Locate every blood parasite and identify its species.
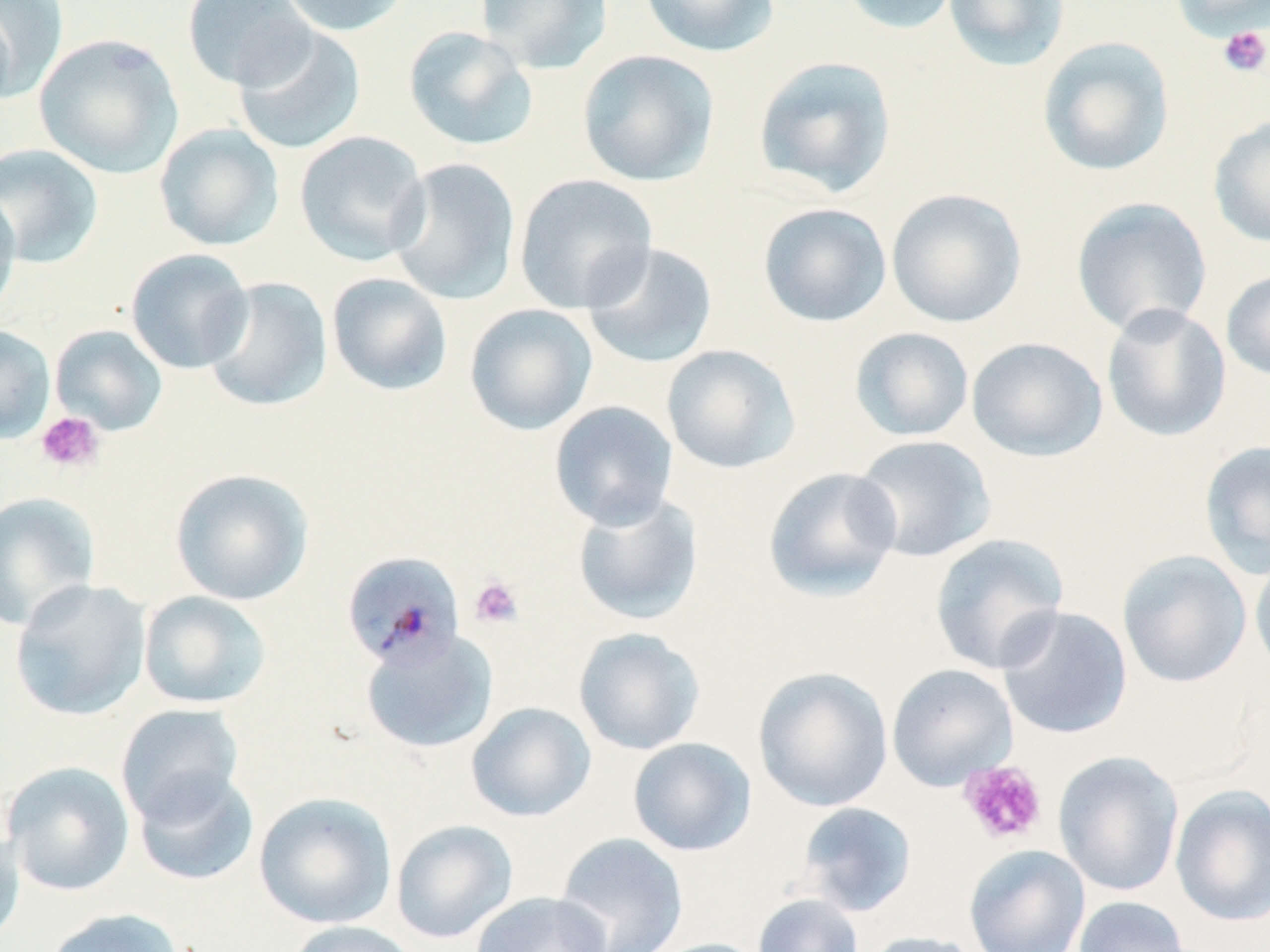
Approximate bounding boxes as [x1, y1, x2, y2] in pixels.
Plasmodium malariae-infected red blood cells: [341, 552, 466, 668].
No Plasmodium falciparum, Plasmodium ovale, Plasmodium vivax, Babesia divergens, or Trypanosoma brucei observed.

Summary:
  - Platelet locations: [1217, 25, 1269, 78], [35, 411, 105, 474], [469, 575, 523, 628], [959, 760, 1048, 846]
  - Uninfected red blood cell locations: [1, 0, 68, 101], [182, 0, 317, 91], [276, 0, 413, 37], [475, 0, 614, 75], [638, 0, 781, 58], [837, 0, 963, 36], [943, 0, 1071, 72], [1169, 0, 1270, 42], [0, 7, 16, 111], [232, 23, 367, 155], [403, 26, 539, 152], [34, 33, 183, 179], [1037, 36, 1175, 177], [576, 49, 720, 187], [753, 56, 897, 198], [1208, 114, 1270, 248], [154, 123, 285, 251], [294, 130, 430, 266], [0, 143, 104, 268], [388, 158, 521, 306], [513, 173, 658, 313], [886, 188, 1027, 328], [0, 189, 22, 317], [1071, 197, 1213, 337], [758, 202, 892, 327], [580, 241, 719, 370], [125, 248, 254, 374], [1221, 268, 1270, 383], [327, 272, 453, 396], [201, 276, 333, 413], [464, 303, 598, 435], [1101, 303, 1232, 443], [50, 324, 168, 435], [0, 325, 56, 444], [850, 327, 974, 442], [966, 337, 1108, 462], [661, 344, 801, 474], [549, 400, 678, 530], [852, 434, 997, 563], [1199, 439, 1270, 579], [762, 466, 903, 602], [170, 468, 315, 605], [0, 491, 101, 631], [571, 492, 704, 626], [929, 534, 1070, 675], [1116, 549, 1253, 689], [1249, 549, 1270, 680], [9, 579, 152, 721], [138, 590, 272, 710], [995, 606, 1133, 740], [573, 627, 706, 755], [360, 630, 498, 754], [886, 663, 1018, 790], [752, 666, 893, 813], [466, 702, 596, 822], [115, 703, 245, 825], [628, 737, 757, 856], [1053, 751, 1184, 897], [2, 761, 135, 896], [132, 769, 260, 887], [1170, 784, 1270, 926], [253, 792, 396, 929], [797, 802, 918, 917], [391, 819, 518, 944], [0, 828, 26, 947], [555, 832, 689, 952], [963, 844, 1090, 952], [470, 891, 612, 952], [752, 893, 864, 952], [1073, 895, 1192, 952], [42, 907, 184, 952], [282, 920, 423, 952], [860, 931, 987, 952], [643, 938, 775, 952]
  - Slide-level diagnosis: Plasmodium malariae
  - Magnification: 1000x
  - Modality: optical microscopy
  - Image size: 1270×952 pixels
  - Preparation: thin blood smear
  - Stain: May-Grünwald-Giemsa
  - Field of view: one of a larger specimen